Report the malaria status of this cell.
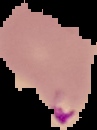

Parasitized.

image type = segmented cell region on a black background
preparation = thin blood smear
image size = 97×130 pixels